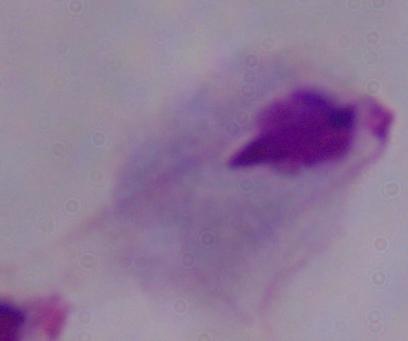 1000x magnification. Photomicrograph. A trichomonad is seen.